Classify this cell by malaria status.
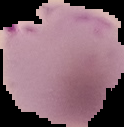
It is parasitized.

{
  "image_type": "cell region segmented out of the field of view; surrounding area masked to black",
  "image_size": "124×127 pixels",
  "preparation": "thin blood smear"
}